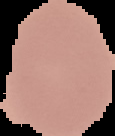

{
  "image_size": "115×136 pixels",
  "image_type": "cell region segmented out of the field of view; surrounding area masked to black",
  "malaria_status": "uninfected",
  "preparation": "thin blood smear"
}